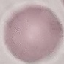

Result: no malaria parasites detected. Photographed with a smartphone camera at the microscope eyepiece. Giemsa stain. Cell patch, automatically extracted from a larger field of view and resized to 64 × 64 pixels. Thin blood film.